Outline each Plasmodium falciparum-infected red blood cell.
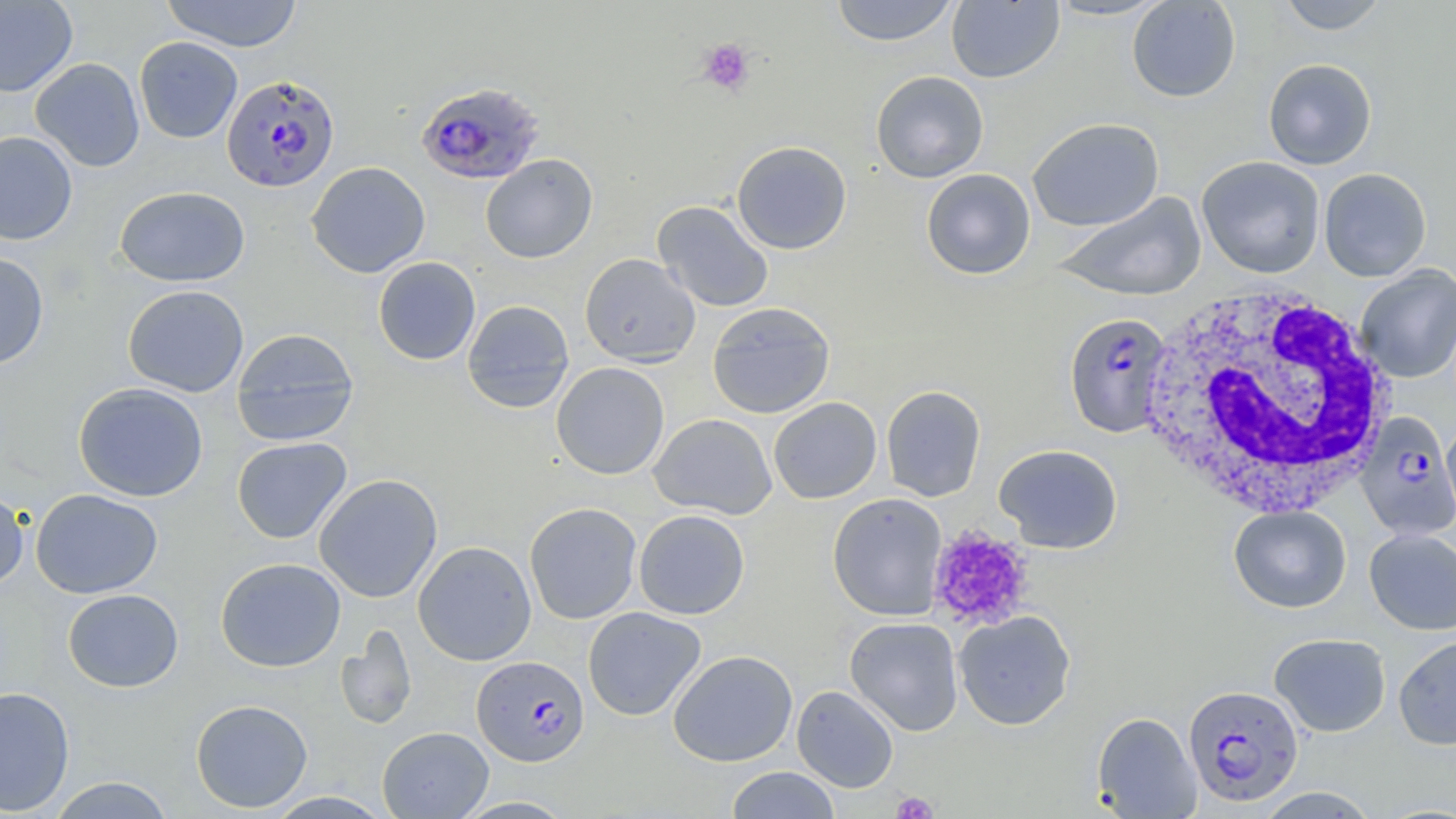
Approximate bounding boxes as (x1, y1, x2, y2) in pixels.
Plasmodium falciparum-infected red blood cells: (222, 74, 340, 191), (414, 81, 547, 186), (1063, 312, 1173, 437), (1355, 411, 1456, 540), (472, 655, 589, 767), (1183, 684, 1304, 806).

Summary:
  - Uninfected red blood cell locations: (0, 0, 78, 97), (160, 0, 303, 52), (830, 0, 959, 46), (946, 0, 1064, 83), (1045, 0, 1171, 21), (1127, 0, 1241, 102), (1276, 0, 1389, 34), (134, 36, 243, 143), (30, 57, 145, 172), (1263, 58, 1377, 170), (870, 70, 989, 183), (1027, 117, 1164, 231), (0, 131, 78, 245), (732, 140, 852, 254), (481, 154, 598, 263), (1196, 156, 1326, 278), (306, 161, 431, 278), (921, 168, 1036, 279), (1319, 168, 1432, 282), (114, 185, 250, 287), (1053, 192, 1207, 301), (652, 200, 774, 313), (0, 251, 49, 370), (579, 253, 701, 367), (373, 257, 481, 365), (1355, 264, 1456, 383), (122, 284, 249, 397), (462, 299, 574, 413), (707, 302, 835, 419), (231, 328, 360, 446), (551, 362, 669, 479), (72, 382, 209, 502), (881, 385, 985, 502), (768, 397, 882, 504), (649, 413, 777, 519), (1441, 420, 1456, 524), (231, 437, 352, 544), (994, 443, 1123, 553), (313, 474, 442, 603), (0, 485, 30, 590), (30, 488, 163, 598), (827, 493, 947, 620), (524, 502, 643, 624), (1228, 505, 1351, 613), (633, 509, 750, 619), (1364, 529, 1456, 635), (413, 540, 537, 666), (215, 557, 346, 672), (62, 588, 184, 692), (582, 607, 706, 721), (953, 610, 1076, 730), (844, 616, 964, 736), (335, 625, 417, 731), (1269, 633, 1391, 737), (1393, 634, 1456, 750), (668, 649, 798, 766), (792, 685, 899, 792), (0, 686, 75, 816), (190, 699, 313, 813), (1092, 711, 1201, 818), (377, 727, 494, 818), (726, 767, 840, 819), (47, 776, 176, 818), (1253, 787, 1379, 818), (265, 791, 394, 818), (453, 796, 578, 818)
  - Platelet locations: (697, 38, 756, 96), (927, 525, 1035, 632), (891, 791, 939, 818)
  - White blood cell locations: (1136, 282, 1395, 520)
  - Slide-level diagnosis: Plasmodium falciparum
  - Image size: 1456×819 pixels
  - Stain: May-Grünwald-Giemsa
  - Magnification: 1000x
  - Preparation: thin blood film
  - Modality: light microscopy
  - Field of view: single